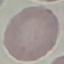
Summary:
  - Result: no malaria parasites seen
  - Preparation: thin blood smear
  - Image type: automatically extracted cell patch, resized to 64 × 64 pixels
  - Stain: Giemsa
  - Capture: smartphone camera at the microscope eyepiece